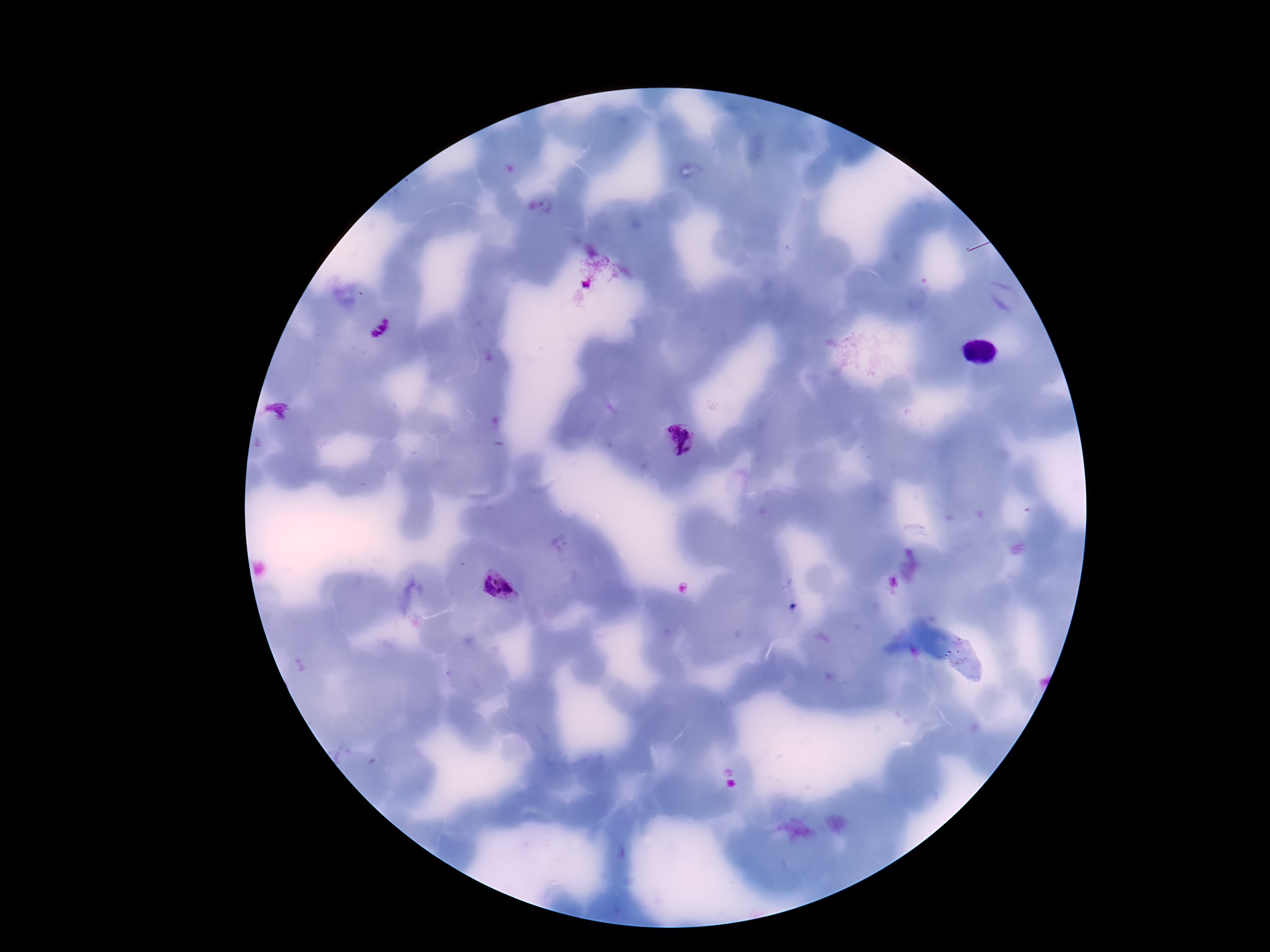

field of view = single
magnification = 100x
patient malaria status = positive
preparation = thick blood smear
stain = Giemsa
Plasmodium parasite locations = approximate centers as [x, y] in pixels: [679, 442], [502, 588]
capture = smartphone camera through the microscope eyepiece
image size = 1270×952 pixels